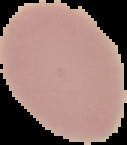
Malaria status: uninfected. From a thin blood smear. The area outside the segmented cell region is set to black. Image is 127×145 pixels.